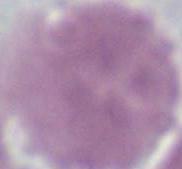

identification = erythrocyte
modality = micrograph
magnification = 1000x